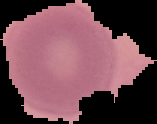
Image is 157×124 pixels. Malaria status: uninfected. From a thin blood film. Segmented cell region on a black background.